Classify this cell by malaria status.
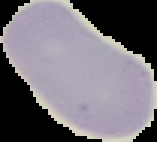
Uninfected.

Summary:
  - Image size: 157×142 pixels
  - Preparation: thin blood film
  - Image type: segmented cell region on a black background